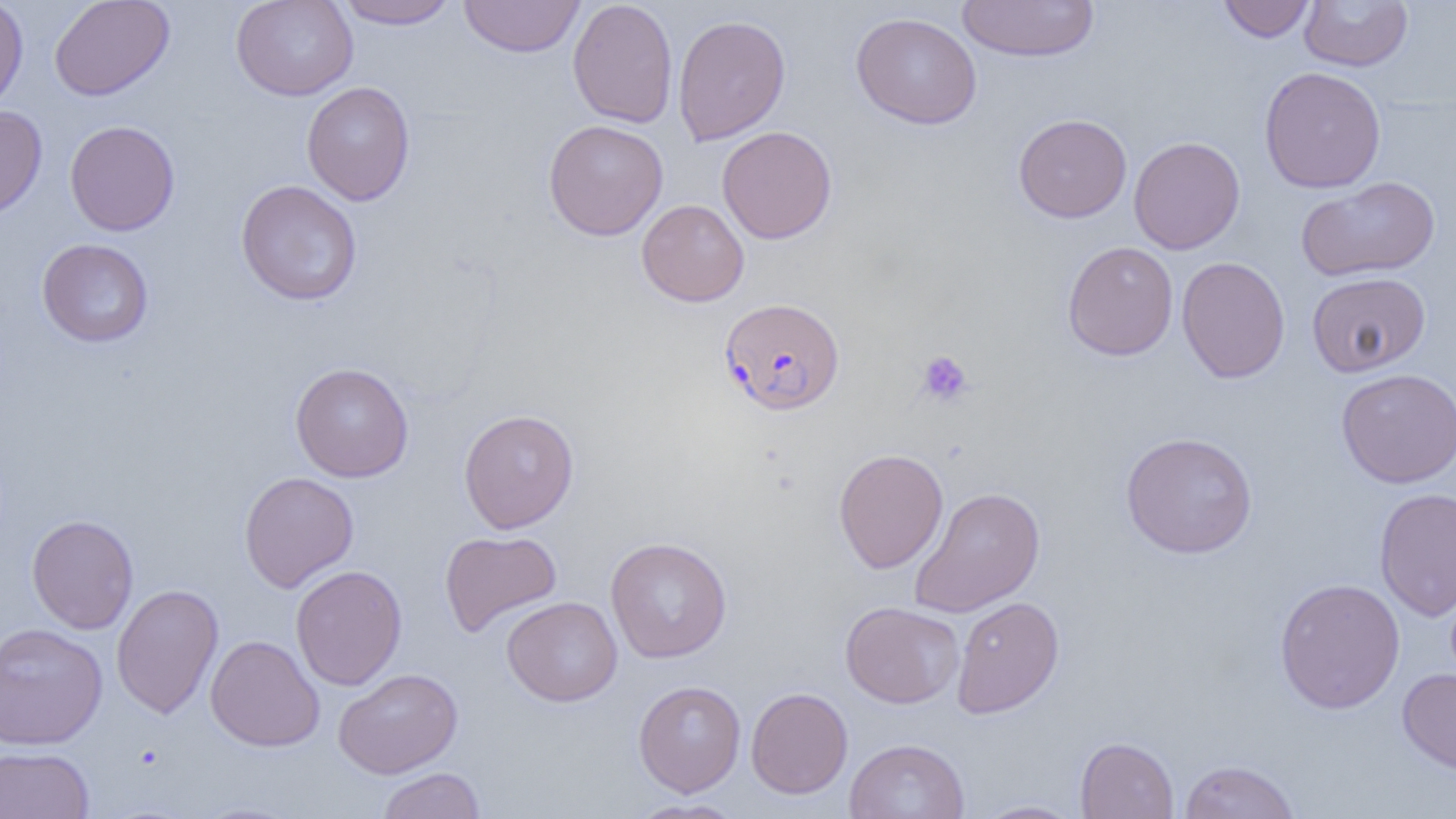

Approximate bounding boxes as (x1, y1, x2, y2) in pixels. Uninfected red blood cell locations: (0, 0, 29, 114), (49, 0, 175, 101), (231, 0, 358, 101), (334, 0, 460, 30), (458, 0, 585, 58), (567, 0, 678, 128), (1218, 0, 1317, 42), (1299, 0, 1413, 72), (957, 1, 1100, 62), (850, 11, 982, 129), (672, 14, 790, 146), (1258, 66, 1386, 193), (301, 81, 415, 206), (0, 105, 48, 222), (1013, 113, 1132, 223), (543, 119, 668, 241), (64, 120, 180, 236), (716, 126, 837, 244), (1128, 136, 1245, 254), (1295, 176, 1441, 282), (236, 179, 363, 305), (637, 199, 749, 306), (37, 238, 154, 347), (1062, 241, 1178, 361), (1176, 256, 1291, 383), (1306, 271, 1431, 377), (290, 362, 415, 482), (1335, 368, 1456, 488), (458, 408, 579, 533), (1120, 431, 1258, 559), (833, 448, 948, 573), (239, 471, 359, 593), (909, 486, 1045, 617), (1374, 487, 1456, 621), (26, 514, 139, 634), (439, 530, 562, 638), (604, 536, 732, 663), (290, 565, 407, 690), (1274, 577, 1405, 714), (111, 584, 224, 719), (502, 596, 623, 706), (951, 596, 1065, 718), (840, 601, 964, 709), (0, 622, 108, 750), (205, 635, 325, 752), (1397, 667, 1456, 776), (333, 668, 462, 778), (633, 680, 746, 797), (745, 687, 854, 799), (1075, 736, 1179, 818), (843, 738, 970, 819), (0, 746, 94, 818), (1179, 759, 1301, 819), (377, 767, 486, 819), (626, 799, 745, 818), (972, 799, 1085, 818), (189, 801, 305, 819). Platelet locations: (916, 349, 975, 407). Plasmodium falciparum-infected red blood cell locations: (719, 297, 845, 415). Slide-level diagnosis: Plasmodium falciparum. Light microscopy. One field of a larger specimen. Image is 1456×819 pixels. 1000x magnification. Thin blood film.